Name the parasite shown.
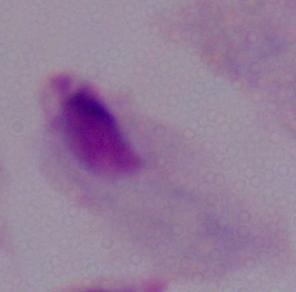
This is a trichomonad.

Summary:
  - Modality: micrograph
  - Magnification: 1000x